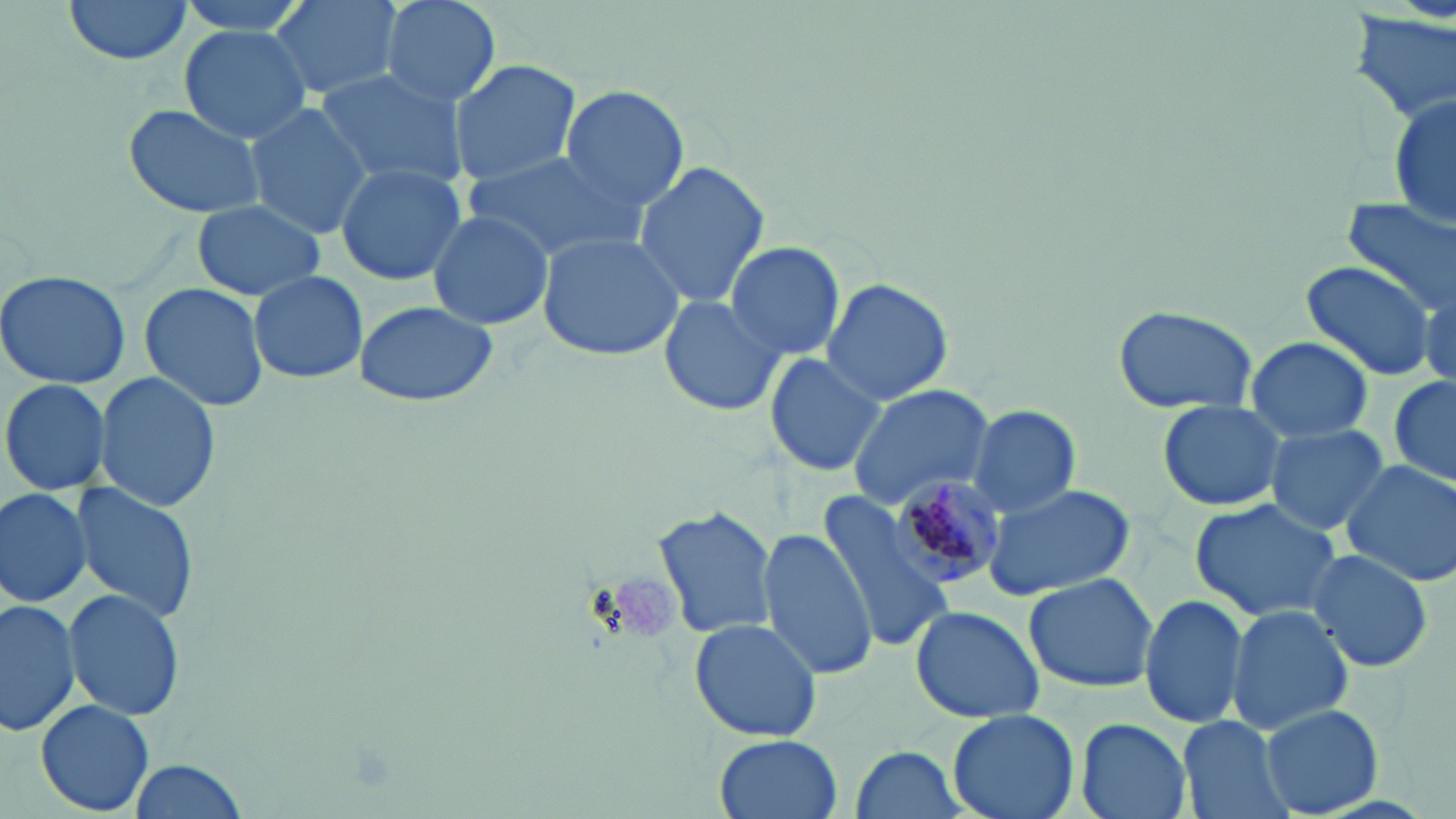
Approximate bounding boxes as (x1, y1, x2, y2) in pixels. Plasmodium malariae-infected red blood cell locations: (885, 477, 1008, 591). Uninfected red blood cell locations: (60, 0, 196, 66), (173, 0, 316, 44), (262, 0, 401, 103), (378, 0, 503, 109), (1349, 3, 1456, 127), (178, 26, 312, 145), (449, 59, 582, 185), (314, 66, 468, 190), (559, 85, 691, 211), (1390, 90, 1455, 230), (120, 101, 267, 220), (242, 102, 376, 239), (464, 149, 647, 262), (632, 159, 772, 310), (332, 162, 467, 284), (1341, 198, 1454, 317), (191, 199, 325, 302), (426, 209, 555, 330), (535, 232, 684, 360), (724, 242, 846, 360), (1301, 259, 1437, 383), (0, 269, 131, 389), (248, 270, 368, 385), (821, 277, 955, 406), (139, 281, 269, 413), (658, 292, 786, 418), (353, 300, 500, 409), (1112, 301, 1262, 411), (1244, 334, 1376, 441), (764, 351, 887, 479), (92, 372, 222, 512), (1389, 374, 1455, 492), (0, 378, 113, 497), (844, 384, 996, 509), (1155, 400, 1292, 514), (966, 403, 1082, 516), (1265, 424, 1389, 534), (1340, 459, 1456, 587), (71, 482, 199, 624), (982, 482, 1136, 600), (0, 485, 92, 610), (815, 492, 957, 653), (1189, 497, 1343, 623), (653, 503, 777, 641), (756, 527, 881, 682), (1305, 547, 1434, 675), (1024, 572, 1160, 694), (63, 589, 184, 722), (1138, 594, 1248, 728), (0, 597, 78, 737), (909, 604, 1044, 724), (1227, 604, 1355, 735), (687, 616, 822, 743), (35, 699, 156, 815), (1259, 705, 1384, 816), (948, 707, 1080, 819), (1075, 717, 1192, 819), (1176, 718, 1295, 819), (714, 734, 843, 819), (844, 746, 972, 819), (128, 759, 249, 817). Slide-level diagnosis: Plasmodium malariae. Captured at 1000x magnification. Image is 1456×819 pixels. Thin blood film. May-Grünwald-Giemsa-stained preparation. One field of a larger specimen. Light microscopy.